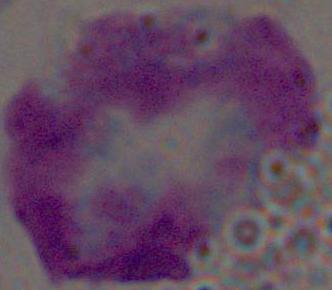

{
  "magnification": "1000x",
  "modality": "photomicrograph",
  "identification": "leukocyte"
}